Assess this cell for malaria.
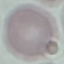
It is uninfected.

preparation: thin smear
stain: Giemsa
image_type: cell patch, automatically extracted from a larger field of view and resized to 64 × 64 pixels
capture: smartphone camera at the microscope eyepiece